Identify the cell.
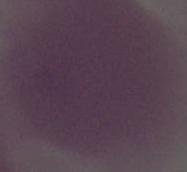

This is an erythrocyte.

Micrograph. 1000x magnification.